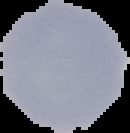
{
  "preparation": "thin blood film",
  "image_size": "130×133 pixels",
  "malaria_status": "uninfected",
  "image_type": "cell region segmented out of the field of view; surrounding area masked to black"
}